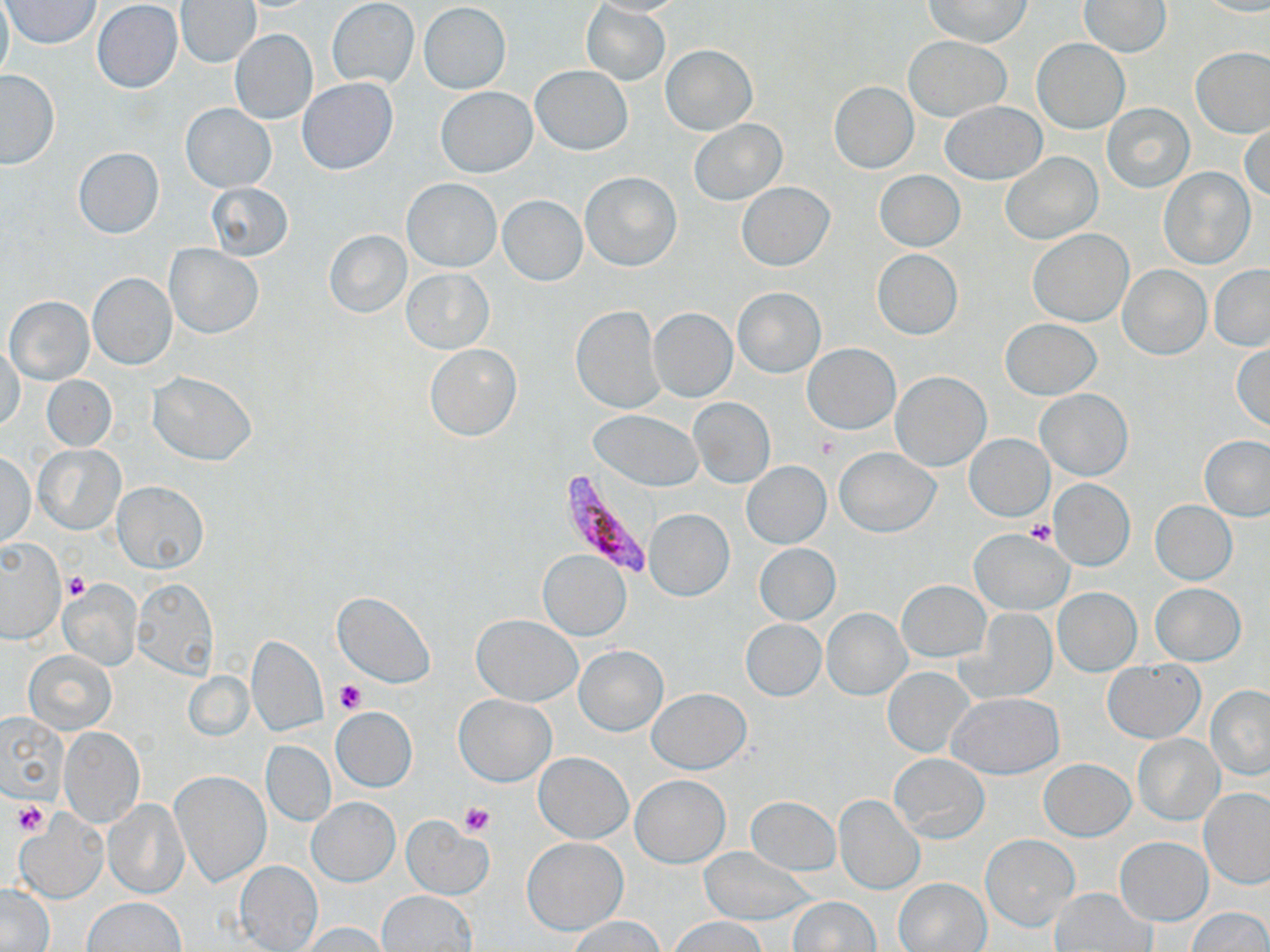

slide-level diagnosis = Plasmodium falciparum
image size = 1270×952 pixels
Plasmodium falciparum-infected red blood cell locations = approximate bounding boxes as [x1, y1, x2, y2] in pixels: [561, 466, 660, 581]
preparation = thin blood film
platelet locations = approximate bounding boxes as [x1, y1, x2, y2] in pixels: [813, 432, 842, 459], [1025, 519, 1057, 546], [63, 572, 90, 602], [334, 678, 366, 713], [13, 802, 50, 837], [460, 803, 495, 837]
magnification = 1000x
modality = optical microscopy
field of view = single
stain = May-Grünwald-Giemsa
uninfected red blood cell locations = approximate bounding boxes as [x1, y1, x2, y2] in pixels: [0, 0, 12, 88], [588, 0, 687, 16], [923, 0, 1031, 47], [1197, 0, 1270, 16], [1, 1, 101, 48], [92, 1, 183, 93], [176, 1, 261, 68], [327, 1, 419, 89], [1079, 1, 1172, 57], [580, 2, 670, 86], [419, 3, 511, 93], [917, 5, 1020, 94], [229, 29, 318, 126], [903, 36, 1013, 121], [1032, 38, 1129, 133], [662, 44, 756, 135], [1191, 46, 1270, 138], [530, 65, 632, 154], [0, 69, 60, 167], [298, 78, 397, 174], [829, 82, 918, 173], [437, 86, 537, 177], [939, 101, 1047, 183], [1103, 103, 1194, 193], [181, 104, 275, 191], [689, 119, 786, 207], [1241, 123, 1270, 203], [72, 147, 165, 239], [1001, 151, 1101, 245], [1159, 167, 1256, 268], [874, 170, 965, 251], [580, 171, 682, 272], [402, 178, 502, 272], [205, 182, 294, 260], [737, 182, 834, 270], [498, 195, 587, 286], [324, 229, 413, 318], [1027, 229, 1133, 326], [165, 244, 263, 338], [872, 249, 962, 340], [1119, 265, 1210, 360], [1209, 265, 1270, 350], [402, 268, 492, 353], [87, 272, 177, 370], [733, 287, 825, 378], [5, 295, 95, 385], [570, 305, 666, 414], [649, 307, 737, 402], [1000, 318, 1102, 400], [1231, 342, 1270, 431], [424, 343, 522, 442], [803, 343, 899, 434], [1, 347, 24, 432], [148, 371, 257, 465], [891, 371, 991, 471], [41, 375, 116, 450], [1037, 389, 1132, 480], [690, 399, 775, 487], [588, 409, 704, 490], [964, 434, 1053, 520], [1200, 435, 1270, 522], [35, 444, 125, 533], [835, 448, 940, 538], [2, 451, 36, 549], [740, 461, 831, 549], [1050, 480, 1134, 569], [114, 481, 208, 573], [1151, 501, 1237, 584], [644, 508, 734, 601], [969, 529, 1072, 614], [0, 539, 65, 643], [754, 543, 841, 625], [538, 550, 630, 639], [59, 579, 142, 671], [133, 579, 218, 677], [897, 579, 989, 663], [1151, 583, 1246, 666], [1053, 588, 1141, 676], [333, 590, 436, 688], [821, 609, 910, 699], [971, 609, 1056, 702], [472, 613, 583, 706], [740, 619, 825, 700], [247, 636, 328, 737], [575, 645, 668, 736], [24, 650, 116, 734], [1103, 659, 1204, 743], [882, 667, 975, 757], [183, 670, 254, 741], [1205, 685, 1269, 780], [648, 688, 751, 773], [948, 692, 1063, 778], [453, 694, 556, 787], [330, 707, 418, 792], [3, 714, 67, 801], [58, 725, 144, 826], [1134, 734, 1223, 825], [262, 741, 335, 824], [535, 752, 632, 843], [890, 753, 989, 842], [1040, 758, 1134, 840], [169, 770, 270, 889], [631, 775, 729, 867], [1200, 787, 1270, 888], [834, 794, 924, 895], [745, 797, 840, 875], [104, 798, 190, 898], [307, 798, 399, 887], [16, 812, 109, 903], [401, 818, 494, 899], [980, 834, 1079, 932], [522, 836, 627, 934], [1116, 837, 1211, 925], [699, 848, 817, 925], [235, 861, 324, 952], [895, 878, 990, 951], [1, 883, 55, 950], [1051, 888, 1156, 951], [378, 890, 477, 951], [788, 896, 879, 950], [83, 897, 186, 951], [1189, 907, 1269, 951], [567, 915, 666, 951], [668, 917, 767, 951], [297, 922, 388, 952]